Assess this cell for malaria.
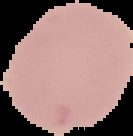

Uninfected.

From a thin blood smear. Image is 133×136 pixels. The area outside the segmented cell region is set to black.